Classify this cell by malaria status.
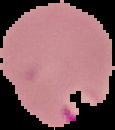
It is parasitized.

Summary:
  - Image type: cell region segmented out of the field of view; surrounding area masked to black
  - Preparation: thin blood smear
  - Image size: 115×130 pixels